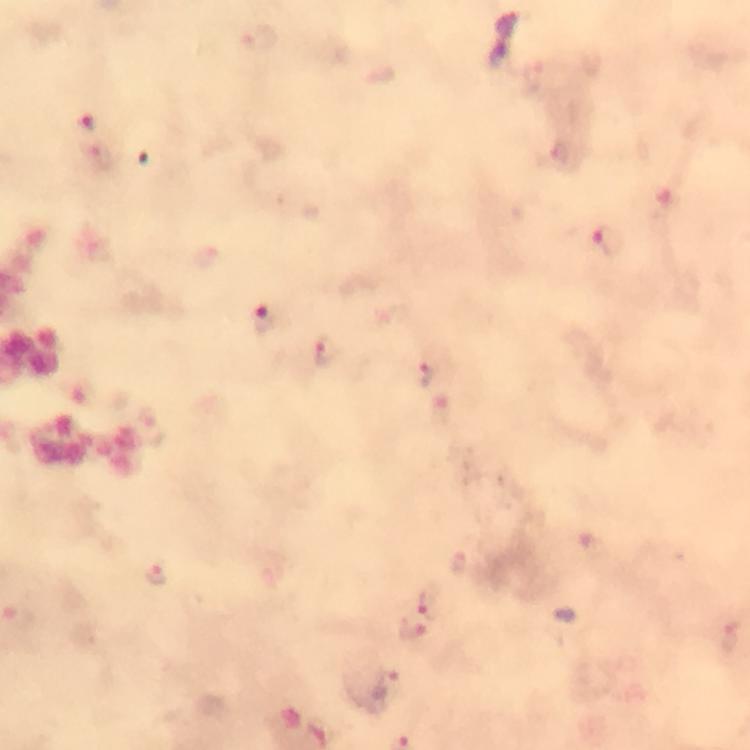 Approximate centers as {x, y} in pixels. Malaria parasite locations: {610, 242}, {270, 319}, {328, 351}, {425, 373}, {157, 576}, {429, 605}, {19, 617}, {411, 631}. Cropped region of a single field of view. At 100x magnification. Giemsa-stained preparation. Immersion oil was used. Image is 750×750 pixels. Photographed with a smartphone mounted on the microscope. Thick blood smear. From a malaria diagnostic workup.